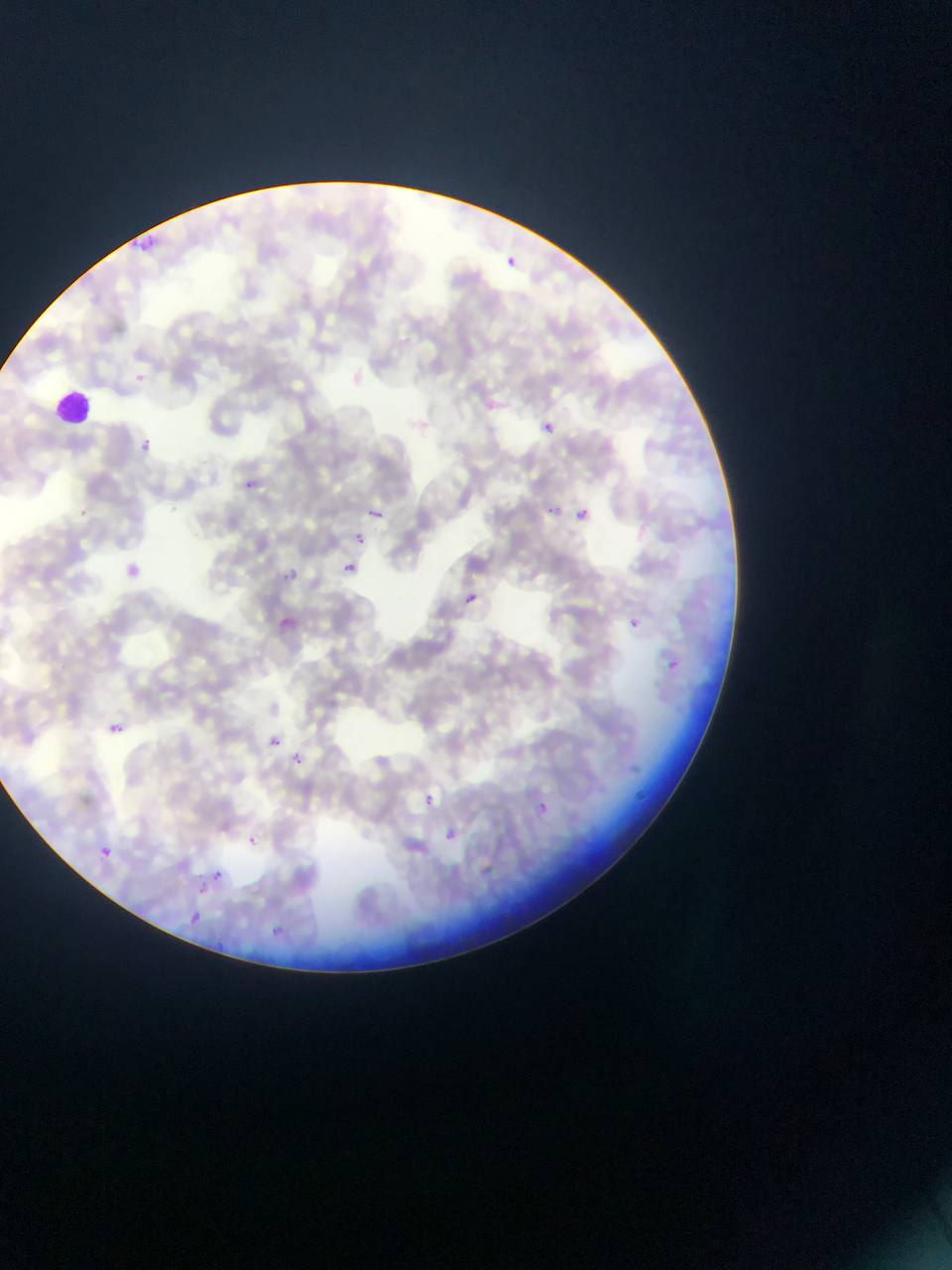
Approximate bounding boxes as [left, top, right, bottom] in pixels.
Summary:
  - Plasmodium parasite locations: [130, 221, 159, 255], [506, 256, 518, 265], [484, 398, 498, 412], [541, 421, 555, 435], [134, 430, 160, 452], [233, 477, 265, 496], [349, 495, 395, 520], [547, 505, 558, 515], [577, 508, 590, 521], [351, 533, 373, 548], [112, 551, 142, 583], [340, 558, 365, 584], [272, 567, 306, 586], [466, 592, 479, 605], [620, 608, 651, 628], [276, 612, 316, 644], [668, 660, 679, 671], [253, 722, 309, 756], [108, 723, 124, 735], [292, 754, 304, 764], [627, 775, 664, 811], [408, 783, 447, 814], [536, 802, 549, 815], [440, 823, 464, 846], [246, 833, 261, 847], [400, 839, 426, 865], [101, 846, 114, 860], [212, 869, 223, 880], [187, 910, 204, 927], [266, 919, 317, 948], [210, 941, 251, 949]
  - Leukocyte locations: [55, 390, 91, 426]
  - Preparation: thin blood smear
  - Country: Ghana
  - Image size: 952×1270 pixels
  - Field of view: single
  - Capture: mobile-phone photograph through a microscope